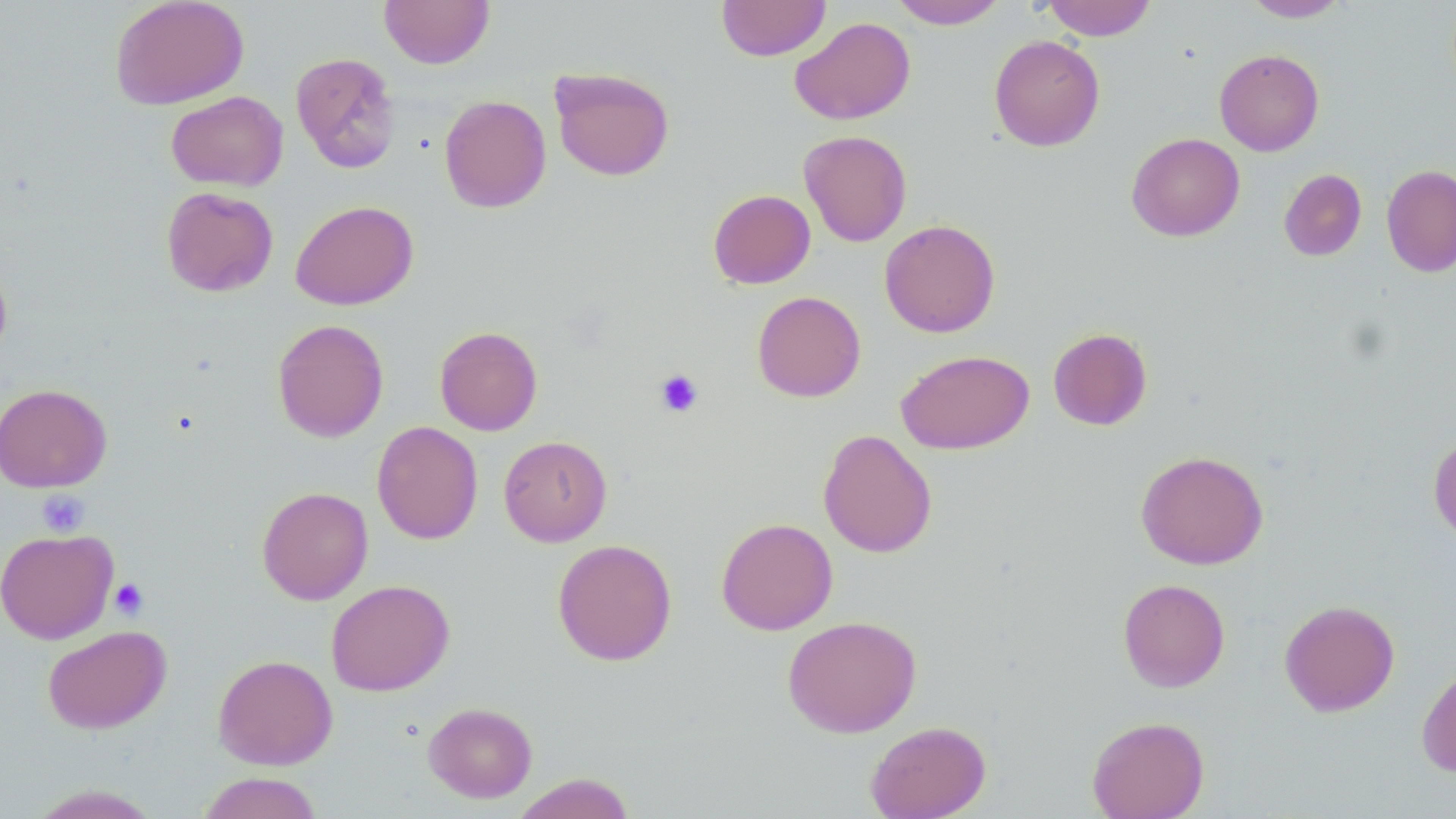

Summary:
  - Coordinate format: approximate bounding boxes as [x1, y1, x2, y2] in pixels
  - Platelet locations: [655, 369, 704, 418], [39, 491, 90, 536], [109, 578, 149, 620]
  - Uninfected red blood cell locations: [110, 0, 249, 110], [379, 0, 494, 69], [717, 0, 830, 61], [889, 0, 1007, 29], [1041, 0, 1157, 41], [1242, 0, 1352, 22], [790, 16, 915, 125], [989, 34, 1105, 151], [1214, 49, 1324, 156], [291, 52, 401, 173], [549, 67, 675, 181], [440, 89, 671, 202], [166, 90, 289, 191], [439, 94, 552, 213], [799, 130, 912, 246], [1126, 132, 1245, 241], [1381, 164, 1456, 277], [1279, 169, 1367, 261], [161, 186, 278, 297], [708, 189, 816, 289], [290, 200, 418, 310], [880, 220, 1000, 337], [0, 255, 12, 364], [752, 291, 866, 402], [272, 319, 389, 442], [434, 326, 543, 436], [1047, 327, 1153, 431], [896, 349, 1034, 454], [0, 383, 112, 493], [371, 421, 483, 544], [818, 429, 938, 558], [1428, 433, 1456, 544], [498, 436, 612, 546], [1135, 450, 1268, 570], [257, 486, 373, 605], [716, 518, 838, 635], [0, 528, 118, 644], [552, 539, 677, 666], [1117, 578, 1230, 692], [326, 579, 454, 696], [1279, 599, 1400, 716], [782, 615, 922, 738], [42, 624, 172, 733], [212, 653, 338, 770], [1416, 663, 1456, 777], [424, 701, 537, 802], [1087, 716, 1209, 819], [865, 720, 991, 819], [196, 772, 324, 819], [512, 773, 636, 819], [26, 784, 164, 818]
  - Slide-level diagnosis: no evidence of blood parasites
  - Field of view: one of a larger specimen
  - Image size: 1456×819 pixels
  - Preparation: thin blood smear
  - Modality: optical microscopy
  - Magnification: 1000x
  - Stain: May-Grünwald-Giemsa